Name the parasite shown.
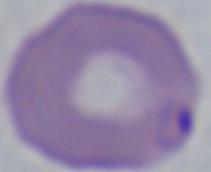

This is Babesia.

Photomicrograph. 1000x magnification.